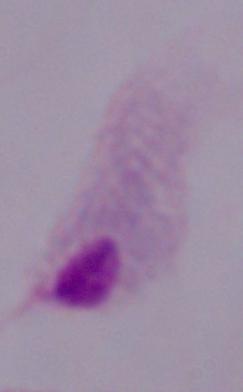

Captured at 1000x magnification. A trichomonad is seen. Photomicrograph.